Assess this cell for malaria.
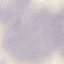
It is uninfected.

Summary:
  - Stain: Giemsa
  - Preparation: thin blood smear
  - Image type: cell patch, automatically extracted from a larger field of view and resized to 64 × 64 pixels
  - Capture: smartphone through the microscope eyepiece